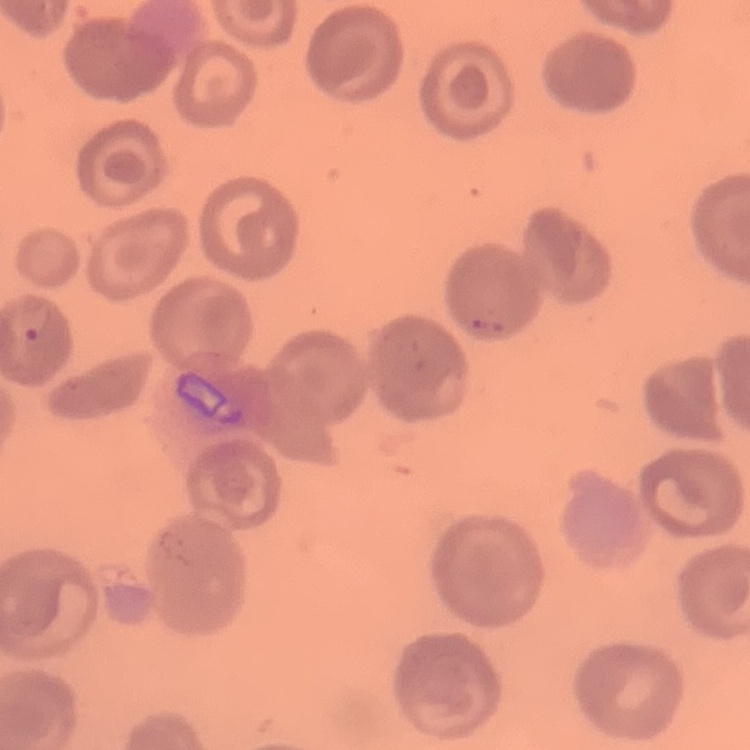
The red blood cells show no rouleaux formation. Field's or Giemsa stain. Square crop of a larger photomicrograph. Thin blood film.